Describe the morphology of the erythrocytes.
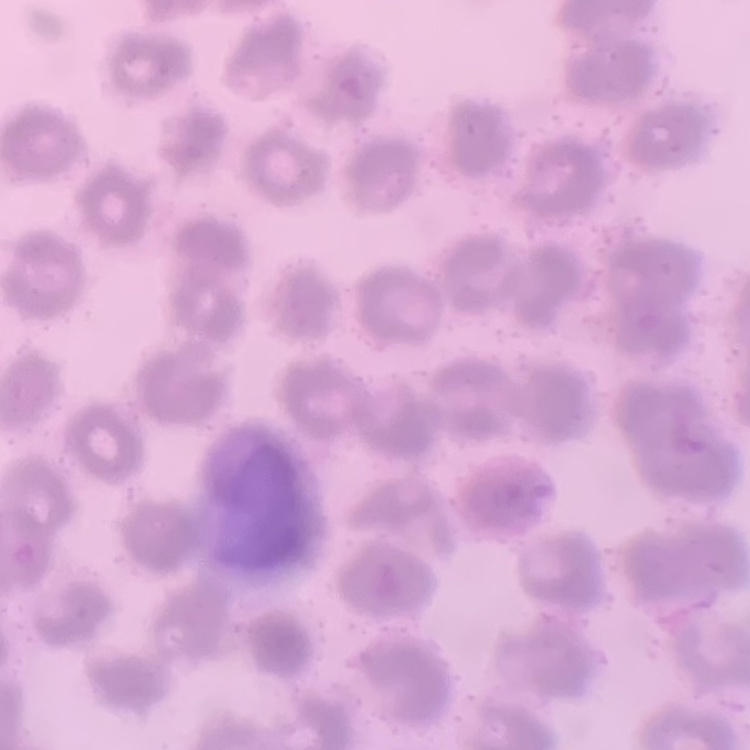

They show no rouleaux formation.

Summary:
  - Image type: one tile cut from a larger photomicrograph
  - Preparation: thin blood smear
  - Stain: Field's or Giemsa